Report the malaria status of this cell.
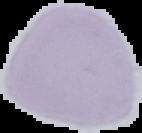

Uninfected.

image size = 142×133 pixels
image type = cell region segmented out of the field of view; surrounding area masked to black
preparation = thin blood smear